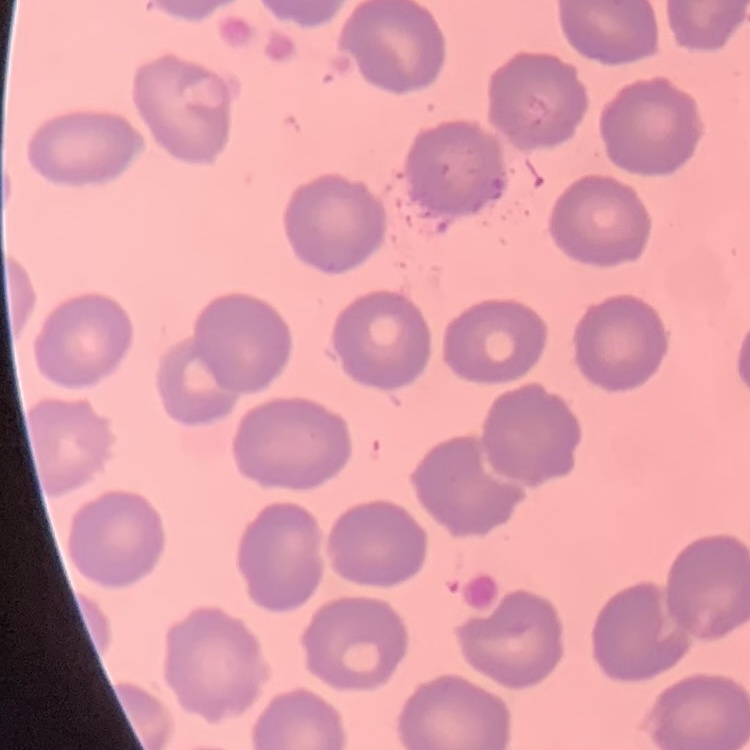

erythrocyte morphology = no rouleaux formation
preparation = thin blood film
image type = one tile cut from a larger photomicrograph
stain = Field's or Giemsa